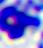
Micrograph. A white blood cell is seen. Captured at 400x magnification.